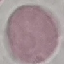
Summary:
  - Malaria status: uninfected
  - Preparation: thin smear
  - Capture: smartphone through the microscope eyepiece
  - Image type: automatically extracted cell patch, resized to 64 × 64 pixels
  - Stain: Giemsa